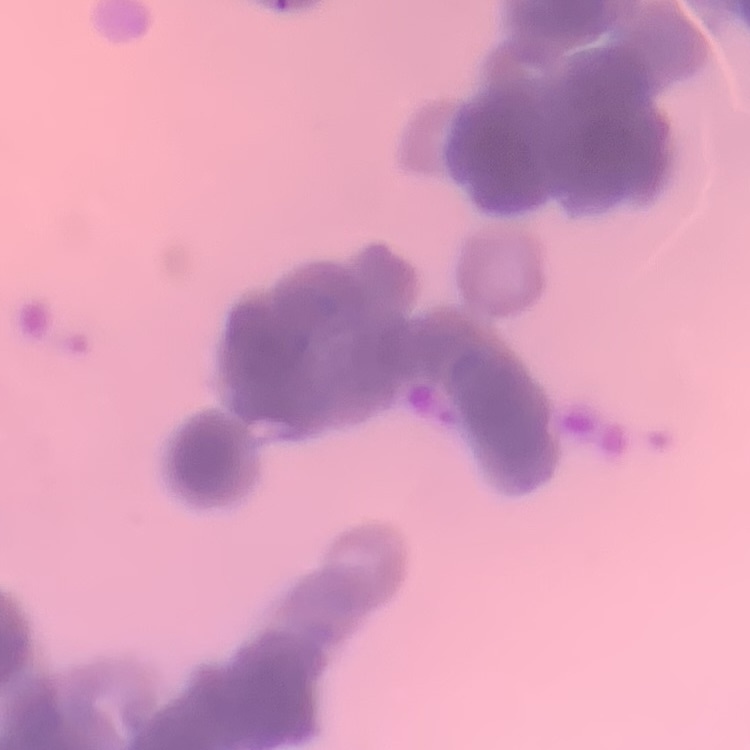

Summary:
  - Erythrocyte morphology: rouleaux formation
  - Image type: square crop of a larger photomicrograph
  - Preparation: thin blood smear
  - Stain: Field's or Giemsa